Assess this cell for malaria.
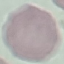

It is uninfected.

preparation = thin blood smear
image type = cell patch, automatically extracted from a larger field of view and resized to 64 × 64 pixels
stain = Giemsa
capture = smartphone camera at the microscope eyepiece